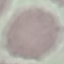

result = no malaria parasites detected
stain = Giemsa
image type = automatically extracted cell patch, resized to 64 × 64 pixels
preparation = thin smear
capture = smartphone through the microscope eyepiece